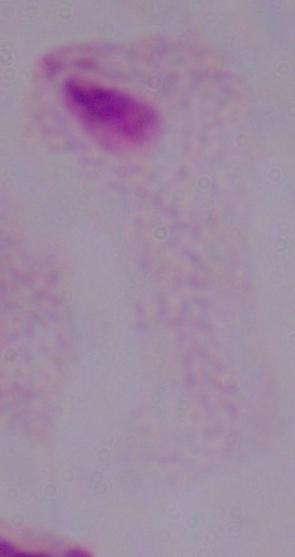
magnification = 1000x
modality = micrograph
identification = trichomonad